Locate every Plasmodium parasite.
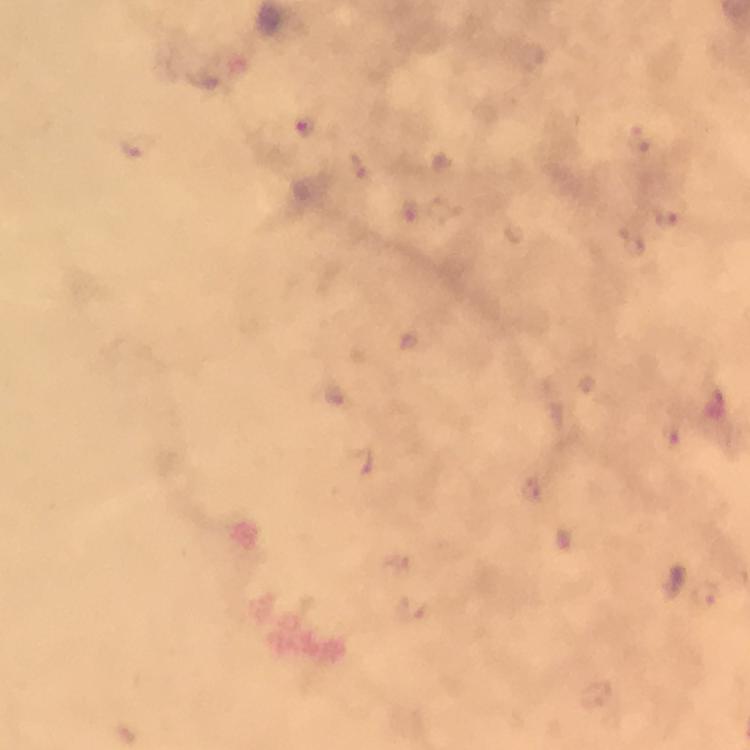

Approximate centers as [x, y] in pixels.
Plasmodium parasites: [305, 128].

Summary:
  - Preparation: thick blood smear
  - Image size: 750×750 pixels
  - Stain: Giemsa
  - Cropped from: one field of view
  - Immersion oil: used
  - Capture: smartphone mounted on the microscope
  - Magnification: 100x
  - Context: from a diagnostic examination for malaria